Name the blood parasite species.
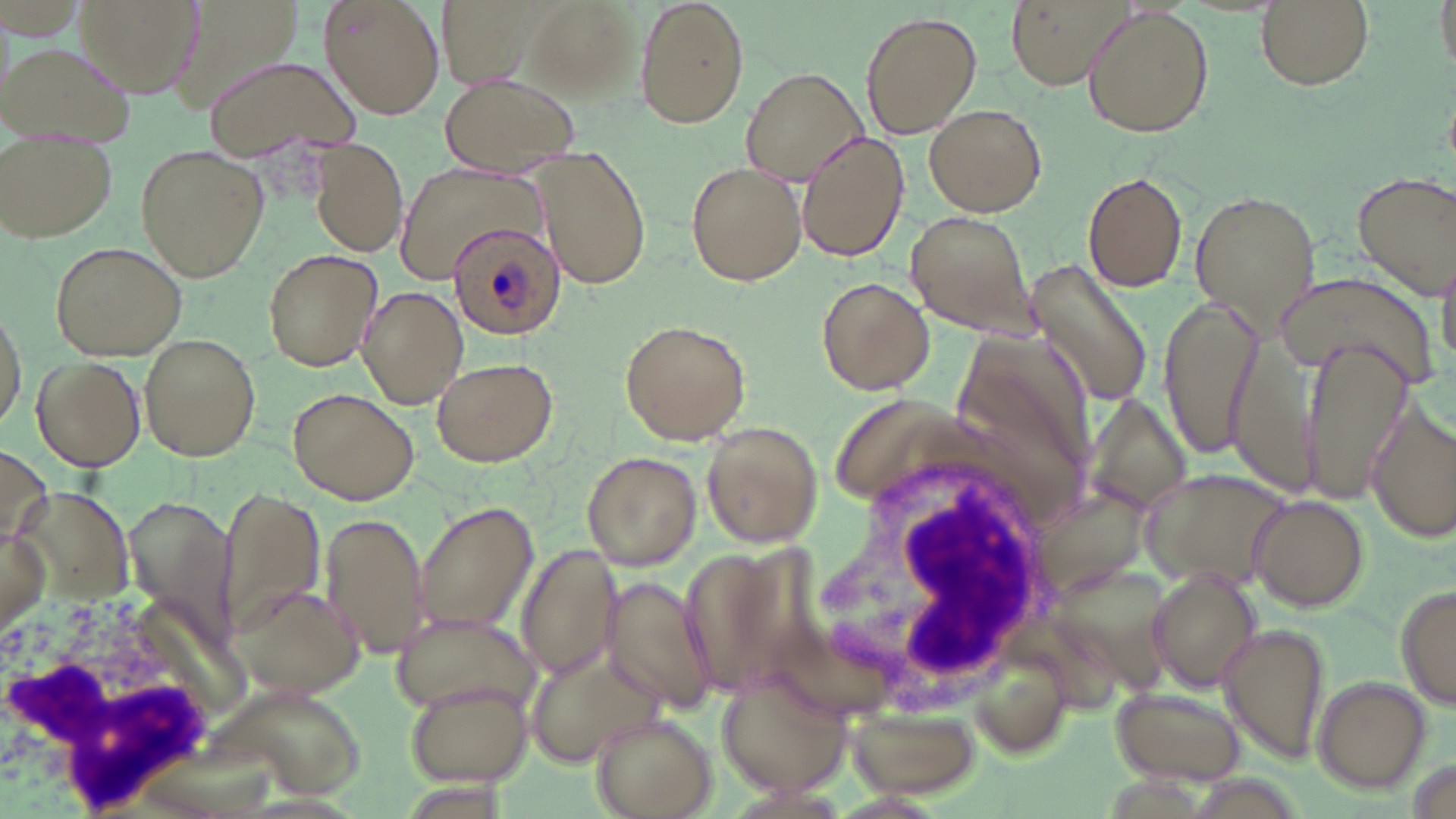

Plasmodium ovale.

Approximate bounding boxes as (x1, y1, x2, y2) in pixels. White blood cell locations: (805, 448, 1070, 708), (0, 585, 238, 817). Uninfected red blood cell locations: (73, 0, 204, 100), (171, 0, 302, 117), (319, 0, 446, 120), (438, 0, 536, 92), (517, 0, 642, 100), (635, 0, 750, 128), (1006, 0, 1131, 88), (1254, 0, 1374, 90), (1081, 5, 1213, 138), (862, 12, 980, 137), (1, 41, 135, 146), (204, 55, 363, 164), (740, 68, 869, 184), (438, 73, 582, 178), (923, 104, 1047, 217), (796, 129, 909, 262), (2, 135, 119, 247), (307, 137, 408, 258), (134, 145, 269, 281), (530, 150, 654, 291), (685, 160, 807, 285), (396, 162, 542, 283), (1081, 169, 1189, 292), (1351, 170, 1456, 299), (1050, 179, 1176, 380), (1190, 188, 1323, 328), (904, 210, 1042, 337), (50, 241, 187, 359), (262, 249, 384, 369), (1024, 260, 1155, 408), (1278, 272, 1437, 386), (816, 275, 935, 395), (357, 286, 469, 408), (1158, 295, 1264, 459), (0, 301, 27, 436), (619, 319, 751, 445), (1220, 329, 1324, 499), (953, 333, 1092, 504), (138, 335, 262, 460), (1302, 338, 1411, 505), (30, 355, 144, 470), (431, 356, 559, 466), (287, 386, 421, 505), (1085, 394, 1191, 513), (832, 397, 996, 504), (1365, 399, 1455, 545), (700, 420, 824, 547), (1, 442, 53, 556), (582, 450, 703, 570), (1139, 468, 1296, 590), (1033, 486, 1147, 597), (221, 488, 324, 641), (21, 489, 129, 595), (1247, 493, 1369, 610), (412, 500, 539, 636), (320, 512, 430, 658), (2, 527, 48, 636), (679, 542, 835, 700), (516, 545, 621, 681), (1043, 565, 1174, 693), (1148, 566, 1264, 693), (599, 576, 719, 716), (229, 581, 367, 699), (1394, 581, 1456, 710), (388, 608, 537, 715), (1217, 622, 1331, 765), (521, 641, 663, 770), (980, 654, 1072, 760), (717, 664, 848, 802), (403, 676, 534, 787), (1312, 677, 1432, 793), (1106, 686, 1247, 789), (845, 703, 984, 798), (590, 710, 717, 818). Plasmodium ovale-infected red blood cell locations: (446, 220, 568, 340). Image is 1456×819 pixels. Thin blood smear. May-Grünwald-Giemsa-stained preparation. Light microscopy. Captured at 1000x magnification. Single field of view.